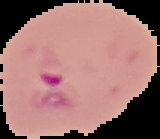

The area outside the segmented cell region is set to black. Malaria status: parasitized. Image is 160×139 pixels. From a thin blood film.